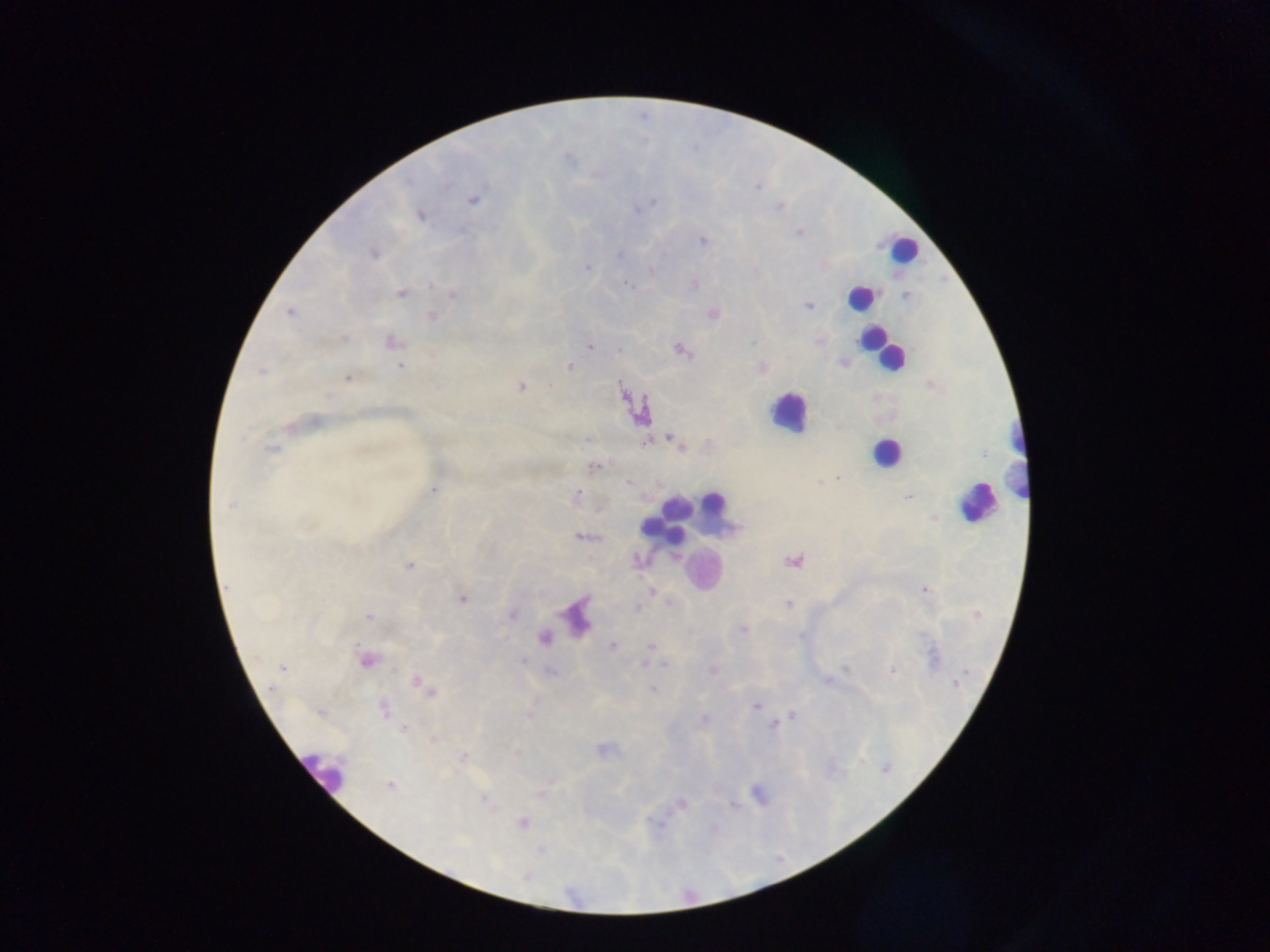

capture = mobile-phone photograph through a microscope
image size = 1270×952 pixels
field of view = single
country = Ghana
preparation = thick blood film
malaria parasite locations = approximate centers as {x, y} in pixels: {568, 159}, {407, 182}, {758, 188}, {473, 199}, {653, 201}, {779, 207}, {638, 209}, {420, 215}, {797, 232}, {703, 240}, {374, 254}, {619, 255}, {587, 268}, {650, 269}, {695, 284}, {628, 285}, {400, 292}, {453, 293}, {905, 295}, {808, 305}, {288, 312}, {713, 314}, {432, 317}, {345, 338}, {818, 340}, {391, 341}, {753, 342}, {590, 347}, {620, 350}, {680, 350}, {571, 366}, {400, 367}, {762, 367}, {261, 372}, {347, 378}, {520, 386}, {437, 387}, {328, 396}, {315, 420}, {290, 427}, {588, 438}, {674, 441}, {682, 448}, {271, 449}, {984, 454}, {593, 466}, {838, 477}, {628, 482}, {433, 490}, {576, 496}, {909, 496}, {230, 505}, {581, 537}, {640, 560}, {793, 561}, {409, 565}, {923, 590}, {652, 591}, {463, 598}, {670, 604}, {788, 604}, {638, 608}, {511, 613}, {369, 617}, {742, 629}, {545, 637}, {612, 645}, {651, 646}, {367, 660}, {523, 660}, {665, 664}, {282, 667}, {892, 670}, {713, 671}, {827, 680}, {956, 683}, {420, 684}, {428, 689}, {653, 689}, {756, 706}, {384, 709}, {793, 715}, {704, 719}, {774, 726}, {403, 729}, {517, 753}, {463, 755}, {885, 769}, {390, 785}, {483, 798}, {682, 803}, {522, 822}
leukocyte locations = approximate centers as {x, y} in pixels: {903, 249}, {860, 297}, {869, 340}, {879, 349}, {788, 412}, {1018, 432}, {886, 452}, {1012, 477}, {712, 503}, {977, 503}, {676, 508}, {667, 523}, {704, 571}, {322, 771}